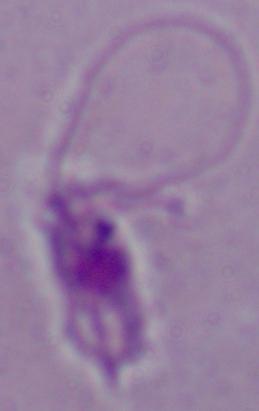
Summary:
  - Identification: Leishmania
  - Magnification: 1000x
  - Modality: photomicrograph